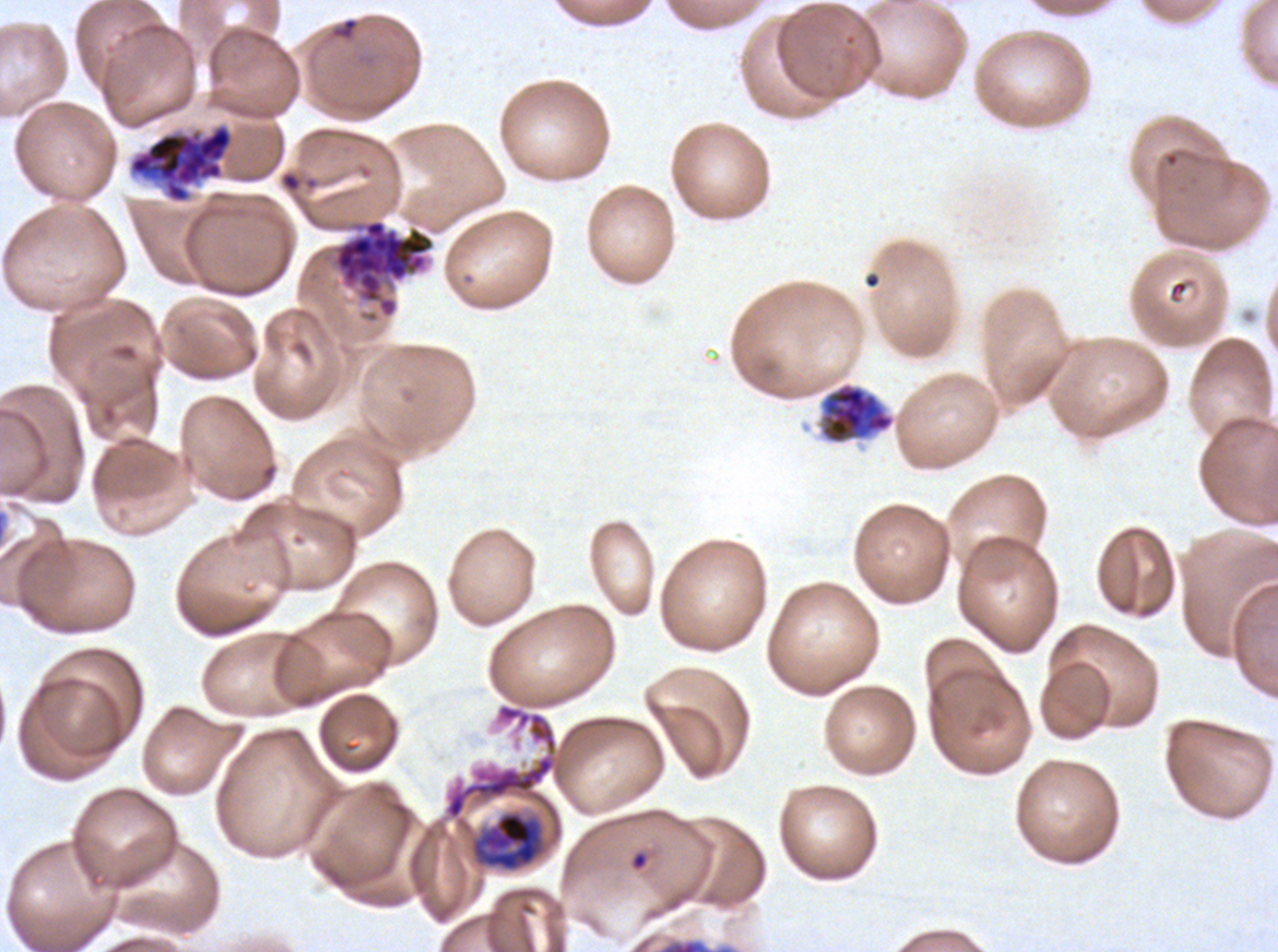
Approximate bounding rectangles given as corner coordinates in pixels from the top-left.
Summary:
  - Late trophozoite locations: (x1=473, y1=812, x2=543, y2=872)
  - Segmenter locations: (x1=129, y1=125, x2=232, y2=201), (x1=330, y1=218, x2=436, y2=319), (x1=444, y1=702, x2=558, y2=821)
  - Ring locations: (x1=331, y1=17, x2=359, y2=41), (x1=630, y1=850, x2=648, y2=871)
  - Early schizont locations: (x1=819, y1=382, x2=895, y2=445)
  - Life-cycle stages observed: ring, late trophozoite, early schizont, segmenter
  - Field of view: one sub-image of a larger composite
  - Image size: 1278×952 pixels
  - Specimen: Plasmodium falciparum from a patient in The Gambia, cultured ex vivo for 24 to 48 hours
  - Preparation: thin blood film
  - Stain: Giemsa